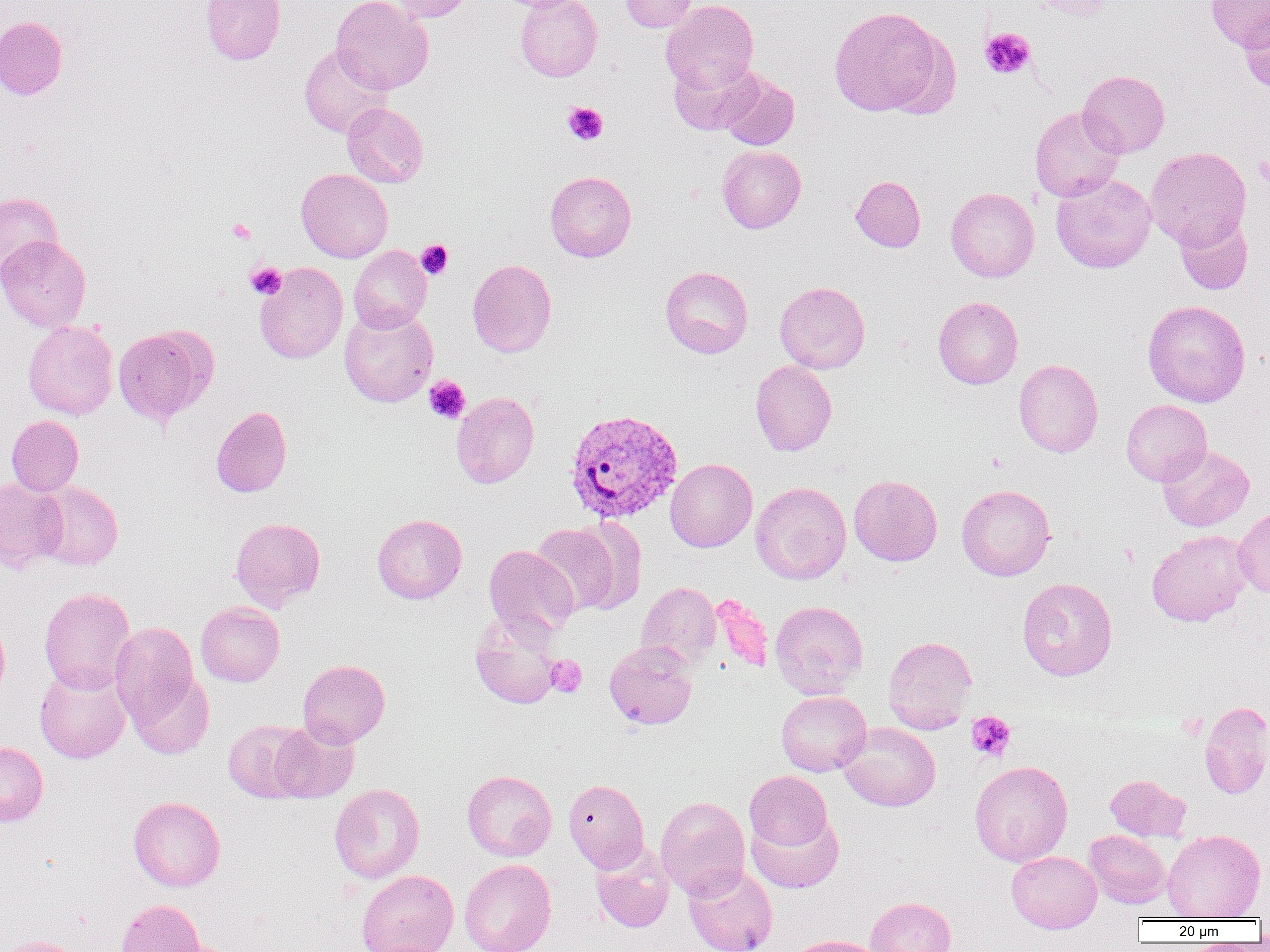

{
  "slide_level_diagnosis": "Plasmodium vivax",
  "modality": "light microscopy",
  "field_of_view": "one of a larger specimen",
  "plasmodium_vivax_infected_red_blood_cell_locations": "approximate bounding boxes as (x1,y1)-(x2,y2) corner pairs in pixels: (565,408)-(683,523)",
  "uninfected_red_blood_cell_locations": "approximate bounding boxes as (x1,y1)-(x2,y2) corner pairs in pixels: (200,0)-(285,65), (331,0)-(434,94), (387,0)-(476,22), (515,0)-(602,81), (619,0)-(700,32), (661,0)-(759,93), (1023,0)-(1114,21), (1206,0)-(1270,51), (828,5)-(948,117), (1239,7)-(1270,95), (0,15)-(67,100), (299,44)-(394,138), (669,58)-(761,135), (717,70)-(800,151), (1077,70)-(1170,157), (342,103)-(428,188), (1030,106)-(1125,202), (716,145)-(806,233), (1147,147)-(1251,250), (296,169)-(393,262), (545,170)-(636,262), (1051,173)-(1156,273), (851,175)-(926,252), (946,187)-(1040,282), (0,192)-(62,284), (1175,214)-(1253,295), (0,235)-(91,332), (348,246)-(432,333), (467,259)-(557,357), (255,262)-(348,363), (660,266)-(753,358), (774,281)-(870,373), (933,296)-(1023,389), (1143,299)-(1251,407), (339,307)-(438,407), (23,321)-(119,420), (113,324)-(218,427), (1014,359)-(1103,458), (751,360)-(837,456), (452,392)-(539,488), (1121,399)-(1211,486), (211,405)-(292,497), (6,415)-(83,496), (1157,444)-(1254,531), (665,458)-(757,552), (849,474)-(942,566), (0,477)-(67,571), (34,481)-(124,570), (751,482)-(851,584), (957,484)-(1055,580), (1233,506)-(1270,598), (372,514)-(467,604), (230,517)-(326,611), (531,523)-(629,616), (1147,530)-(1252,627), (484,545)-(579,637), (1017,577)-(1118,681), (637,581)-(722,668), (38,586)-(136,694), (710,594)-(775,673), (770,600)-(868,699), (196,602)-(284,687), (470,610)-(564,709), (0,614)-(10,705), (110,622)-(200,724), (883,636)-(977,733), (604,640)-(697,730), (298,659)-(390,747), (34,665)-(131,763), (128,671)-(214,760), (776,691)-(871,776), (1200,701)-(1270,800), (269,719)-(359,802), (223,720)-(311,802), (839,722)-(941,811), (0,741)-(48,826), (970,760)-(1073,867), (461,770)-(557,861), (745,771)-(832,852), (1105,775)-(1190,841), (563,779)-(649,873), (329,783)-(425,883), (128,796)-(226,891), (656,796)-(751,900), (747,811)-(844,893), (1162,829)-(1265,920), (1084,830)-(1171,908), (591,844)-(675,933), (1006,851)-(1102,933), (459,859)-(557,952), (684,864)-(777,952), (356,870)-(459,951), (865,896)-(956,952), (116,899)-(205,952), (787,935)-(886,952), (0,936)-(85,952), (156,938)-(243,952)",
  "preparation": "thin blood smear",
  "platelet_locations": "approximate bounding boxes as (x1,y1)-(x2,y2) corner pairs in pixels: (980,28)-(1035,79), (562,102)-(608,145), (1253,156)-(1270,185), (227,218)-(256,243), (416,239)-(453,279), (245,262)-(286,298), (424,375)-(471,424), (546,655)-(587,697), (967,710)-(1016,761)",
  "image_size": "1270×952 pixels",
  "magnification": "1000x"
}